Locate and identify every blood parasite.
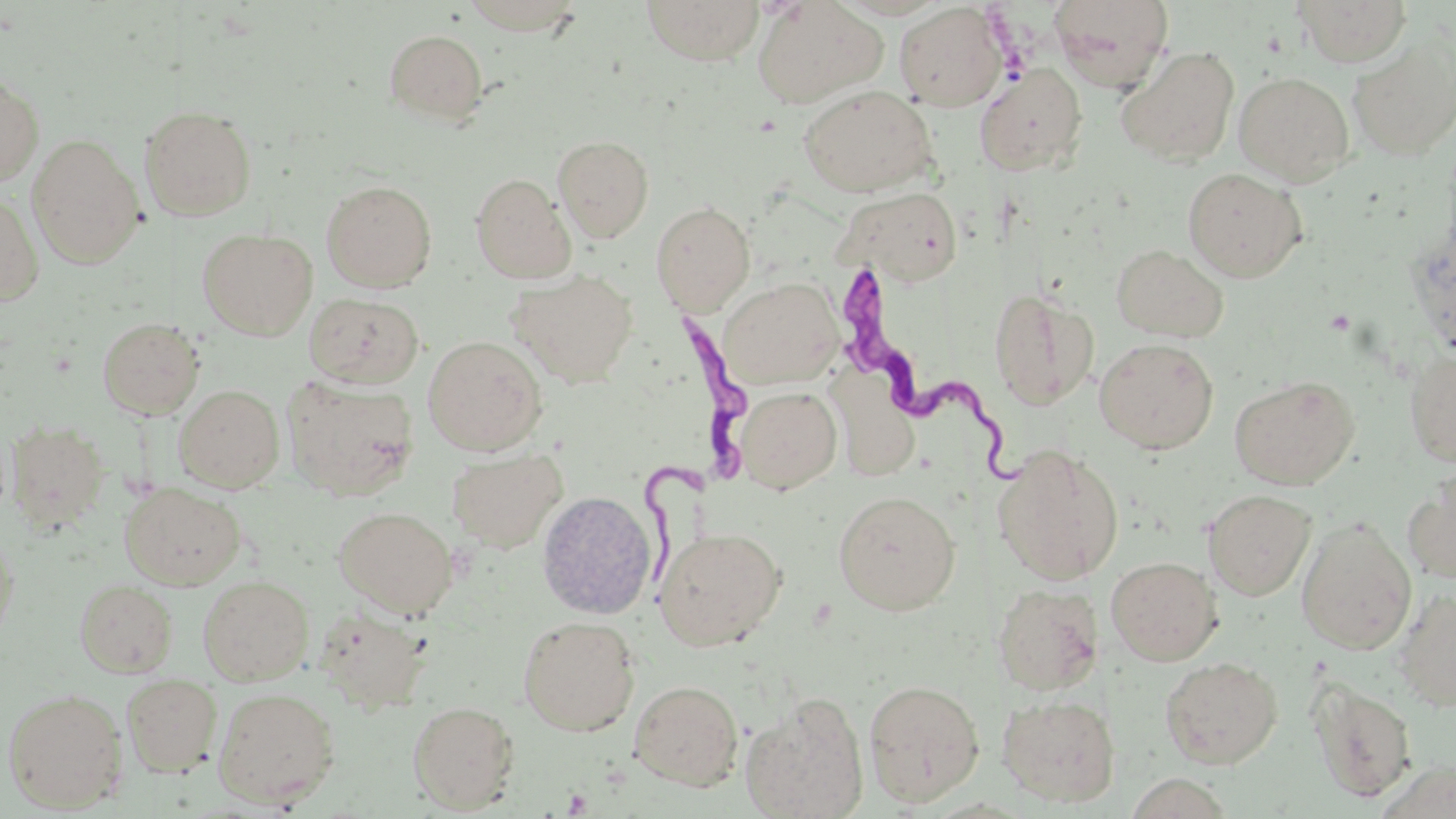

Approximate bounding boxes as (x1, y1, x2, y2) in pixels.
Trypanosoma brucei: (838, 266, 1031, 490), (626, 306, 752, 585).
No Plasmodium falciparum, Plasmodium ovale, Plasmodium malariae, Plasmodium vivax, or Babesia divergens observed.

slide_level_diagnosis: Trypanosoma brucei
stain: May-Grünwald-Giemsa
preparation: thin blood smear
field_of_view: single
image_size: 1456×819 pixels
modality: light microscopy
uninfected_red_blood_cell_locations: 'approximate bounding boxes as (x1, y1, x2, y2) in pixels: (458, 0, 588, 35), (641, 0, 766, 65), (752, 0, 887, 108), (1049, 0, 1175, 91), (1293, 0, 1413, 67), (894, 3, 1008, 112), (384, 29, 488, 125), (1349, 33, 1456, 162), (1116, 46, 1240, 167), (974, 63, 1088, 176), (1233, 71, 1354, 185), (0, 72, 43, 188), (798, 85, 938, 197), (139, 105, 258, 221), (553, 134, 655, 242), (27, 135, 145, 269), (1182, 166, 1307, 283), (470, 173, 575, 284), (321, 179, 437, 292), (836, 186, 965, 287), (0, 189, 44, 307), (651, 201, 755, 314), (198, 228, 318, 340), (1111, 243, 1229, 342), (508, 269, 638, 388), (720, 278, 844, 389), (988, 287, 1099, 411), (304, 292, 424, 389), (97, 316, 205, 419), (423, 335, 548, 455), (1095, 337, 1219, 454), (1404, 349, 1456, 468), (839, 364, 930, 491), (1229, 375, 1359, 490), (282, 377, 419, 500), (174, 384, 285, 494), (735, 385, 841, 494), (5, 418, 110, 532), (992, 444, 1125, 584), (447, 448, 567, 553), (1403, 468, 1456, 584), (119, 483, 246, 590), (1204, 489, 1316, 601), (536, 490, 657, 619), (833, 490, 961, 615), (333, 505, 459, 618), (1297, 518, 1417, 655), (0, 524, 19, 651), (655, 526, 786, 651), (1106, 556, 1222, 665), (197, 575, 314, 686), (75, 579, 177, 678), (992, 583, 1104, 695), (1394, 588, 1456, 711), (315, 605, 435, 713), (517, 615, 640, 736), (1160, 656, 1283, 769), (122, 673, 223, 776), (1308, 677, 1417, 802), (863, 678, 985, 806), (628, 679, 744, 790), (2, 687, 129, 812), (212, 687, 341, 808), (741, 693, 869, 819), (997, 694, 1121, 806), (407, 700, 520, 812)'
platelet_locations: 'approximate bounding boxes as (x1, y1, x2, y2) in pixels: (562, 788, 594, 816)'
magnification: 1000x